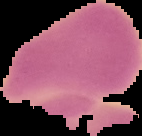
Summary:
  - Malaria status: uninfected
  - Preparation: thin blood smear
  - Image type: segmented cell region with the area outside set to black
  - Image size: 142×136 pixels